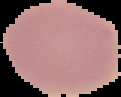 From a thin blood film. Image is 121×97 pixels. Result: no Plasmodium parasites detected. Segmented cell region on a black background.